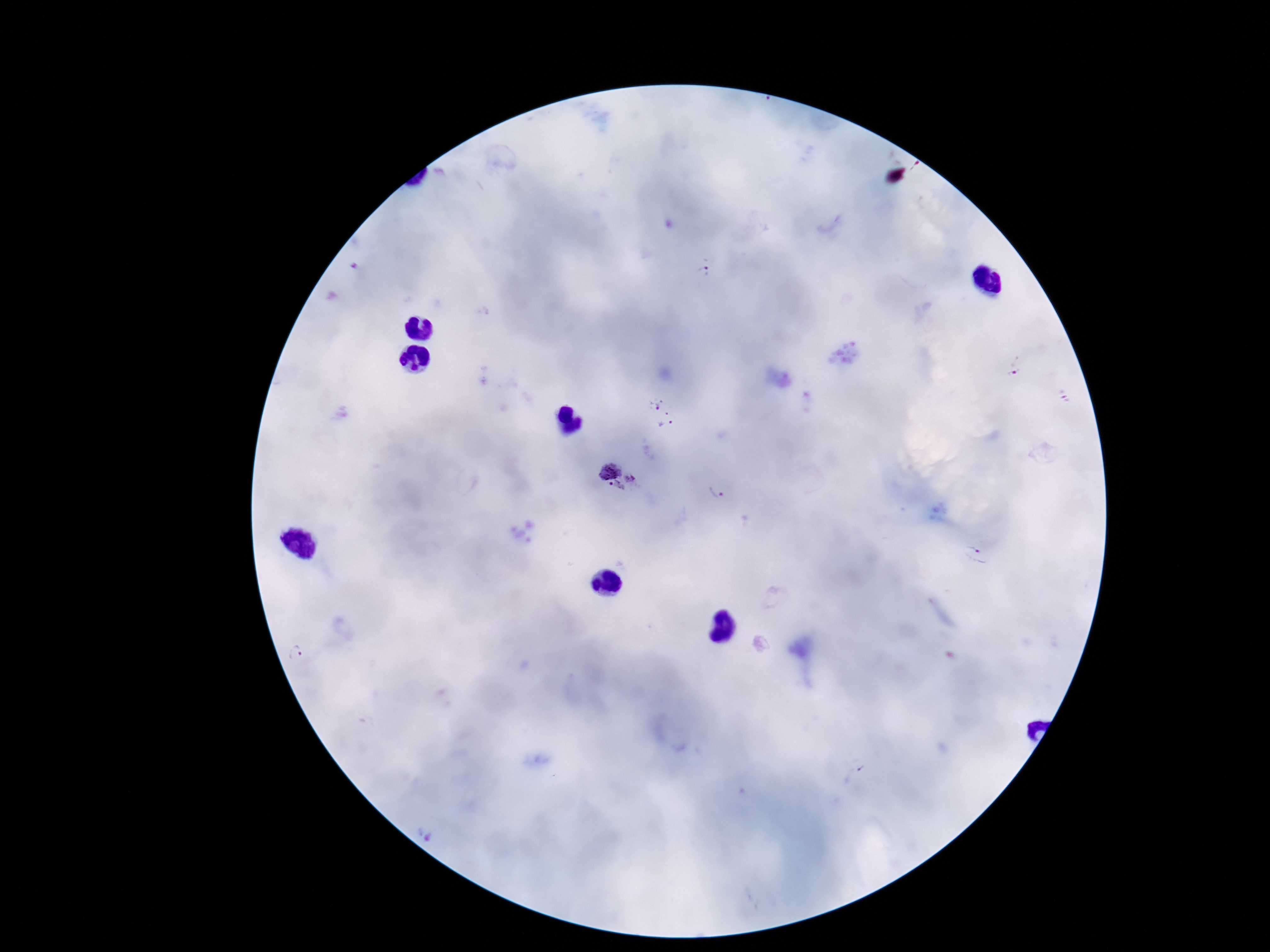

capture = smartphone camera through the microscope eyepiece
stain = Giemsa
Plasmodium parasite locations = approximate object centers, in pixels from the top-left corner: (x=711, y=274), (x=1014, y=366), (x=663, y=414), (x=617, y=476), (x=718, y=496), (x=978, y=556), (x=296, y=654)
magnification = 100x
patient malaria status = infected
field of view = one from this slide
image size = 1270×952 pixels
preparation = thick blood smear